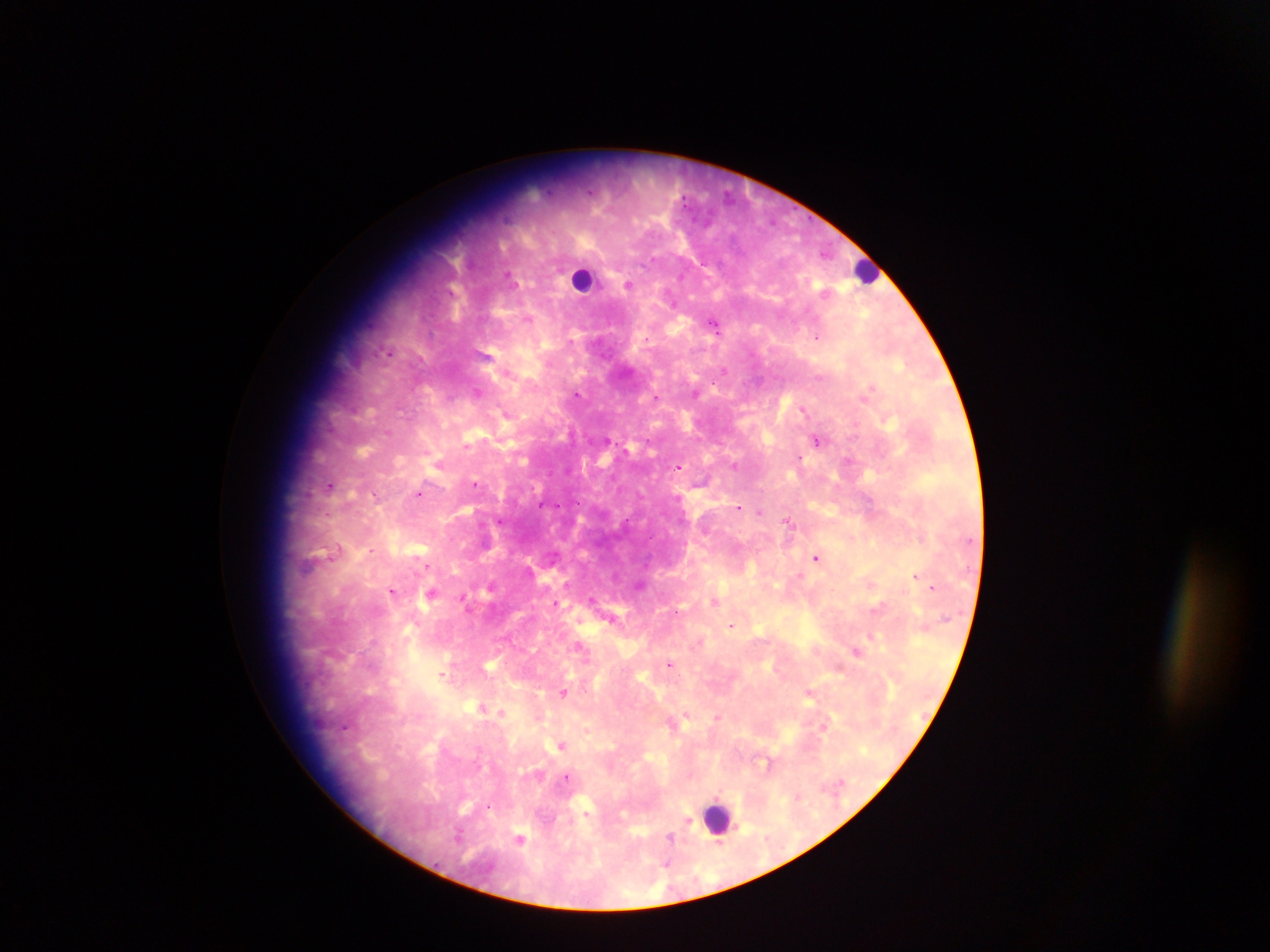
malaria parasite locations = approximate centers as (x, y) in pixels: (651, 260), (508, 274), (628, 284), (528, 318), (715, 326), (817, 336), (571, 342), (388, 352), (507, 370), (724, 370), (818, 377), (712, 385), (871, 388), (477, 392), (577, 395), (656, 398), (803, 409), (506, 413), (855, 425), (387, 432), (817, 440), (465, 446), (800, 458), (847, 460), (735, 466), (679, 467), (475, 483), (330, 485), (375, 494), (419, 494), (577, 502), (542, 504), (738, 507), (759, 512), (327, 514), (787, 520), (500, 521), (371, 549), (336, 550), (816, 557), (427, 567), (915, 575), (932, 587), (392, 590), (431, 593), (591, 598), (462, 599), (715, 601), (555, 603), (876, 608), (611, 619), (731, 625), (872, 636), (581, 646), (856, 651), (670, 664), (442, 674), (563, 693), (809, 695), (482, 707), (502, 712), (687, 715), (717, 717), (824, 725), (344, 728), (561, 745), (767, 764), (566, 777), (489, 808), (688, 822), (459, 835), (521, 838), (669, 838), (719, 843), (666, 863)
image size = 1270×952 pixels
capture = mobile-phone photograph through a microscope
leukocyte locations = approximate centers as (x, y) in pixels: (865, 270), (583, 278), (717, 818)
field of view = single
preparation = thick blood film
country = Ghana